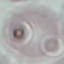
result = no malaria parasites detected
preparation = thin blood film
capture = smartphone camera at the microscope eyepiece
stain = Giemsa
image type = automatically extracted cell patch, resized to 64 × 64 pixels